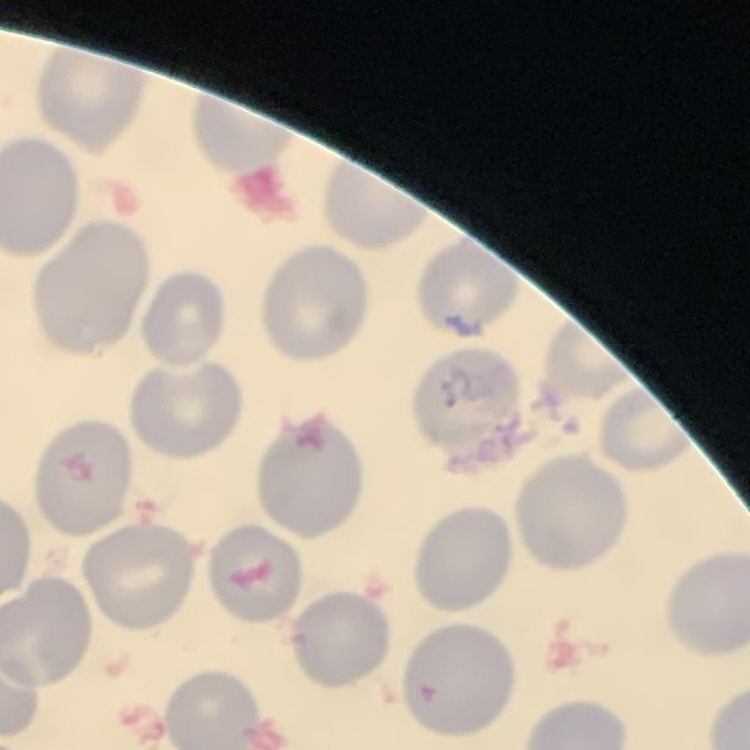 The erythrocytes show no rouleaux formation. Thin peripheral smear. Square crop of a larger photomicrograph. Stained with either Field's or Giemsa.